Report the malaria status of this cell.
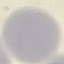
Uninfected.

preparation = thin blood film
stain = Giemsa
image type = automatically extracted cell patch, resized to 64 × 64 pixels
capture = smartphone camera at the microscope eyepiece